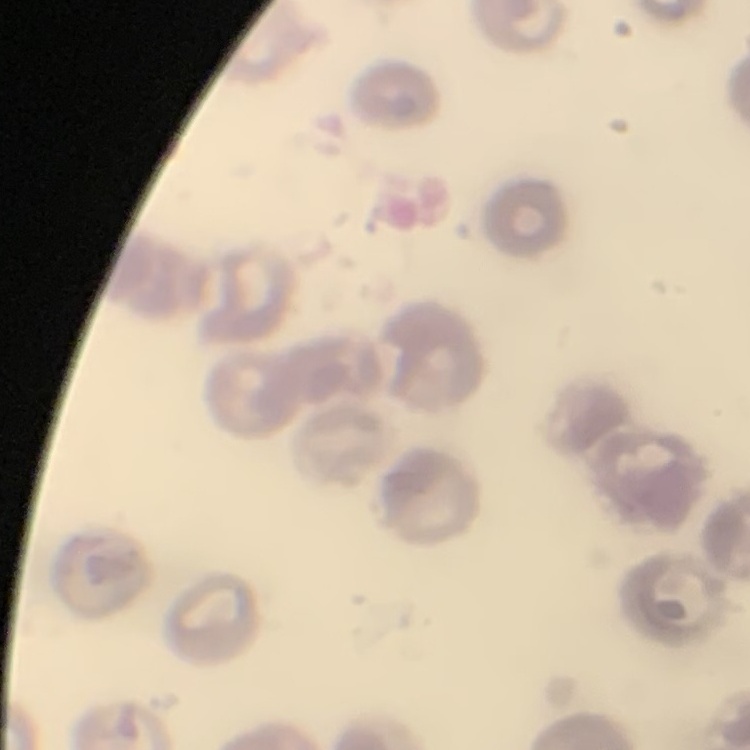

{
  "erythrocyte_morphology": "no rouleaux formation",
  "stain": "Field's or Giemsa",
  "preparation": "thin peripheral smear",
  "image_type": "square crop of a larger photomicrograph"
}